Point out each Plasmodium parasite.
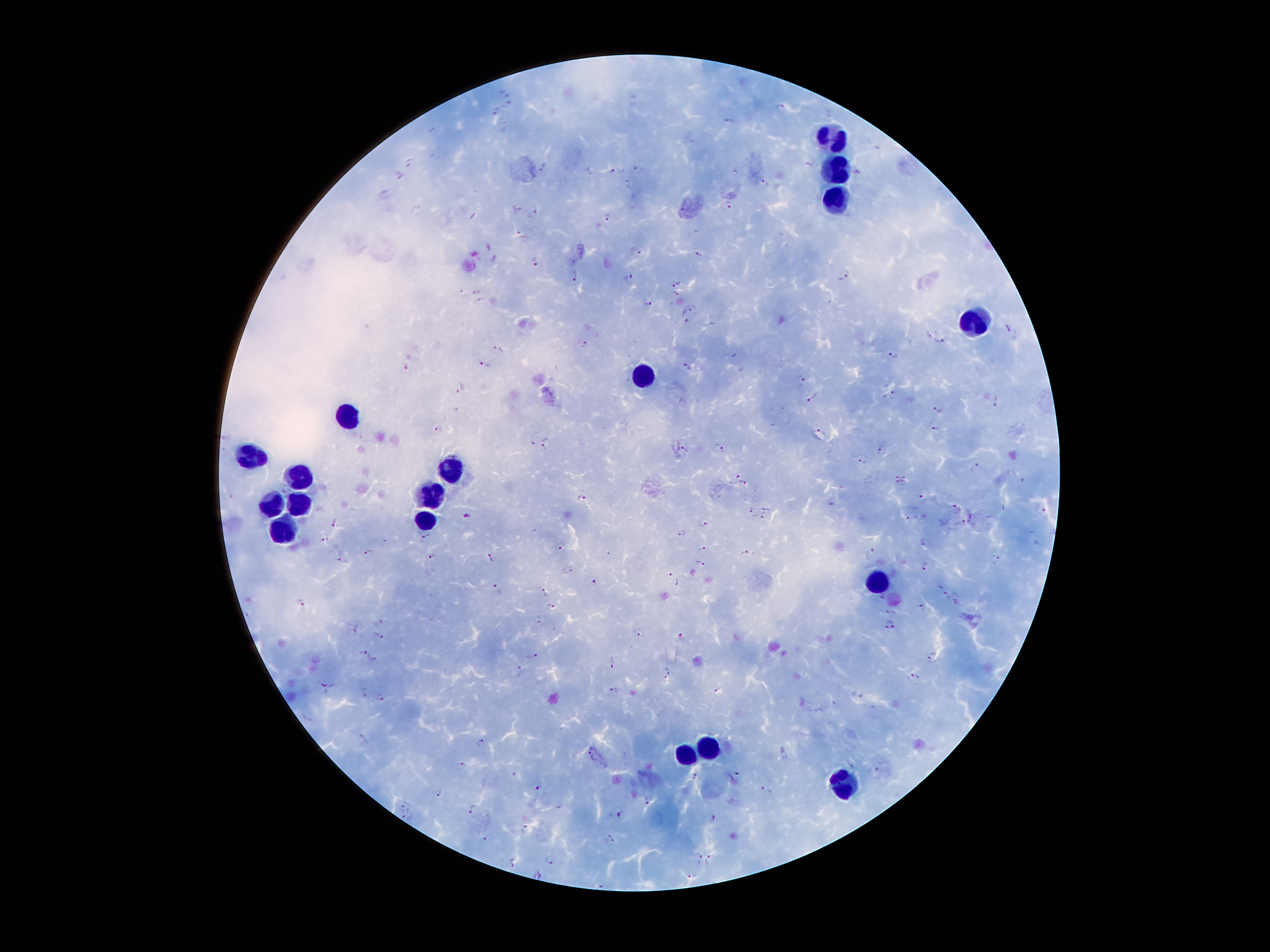
Approximate centers as {x, y} in pixels.
Plasmodium parasites: {506, 92}, {509, 106}, {780, 109}, {495, 111}, {730, 120}, {410, 163}, {810, 164}, {613, 170}, {857, 172}, {764, 182}, {730, 202}, {518, 206}, {535, 210}, {607, 216}, {521, 234}, {638, 252}, {698, 253}, {535, 261}, {844, 272}, {575, 274}, {629, 276}, {676, 283}, {477, 291}, {676, 292}, {649, 303}, {692, 307}, {686, 319}, {943, 341}, {584, 344}, {499, 349}, {894, 355}, {484, 364}, {688, 366}, {405, 367}, {802, 380}, {460, 389}, {894, 394}, {815, 396}, {997, 401}, {939, 407}, {936, 425}, {437, 429}, {818, 432}, {533, 443}, {546, 443}, {719, 446}, {685, 447}, {882, 450}, {863, 457}, {974, 466}, {739, 475}, {900, 478}, {1023, 479}, {744, 483}, {580, 497}, {922, 497}, {832, 502}, {955, 506}, {768, 507}, {1041, 508}, {752, 510}, {468, 515}, {762, 516}, {907, 517}, {333, 521}, {965, 521}, {705, 523}, {681, 533}, {326, 537}, {425, 538}, {924, 542}, {561, 545}, {701, 548}, {874, 548}, {368, 553}, {747, 553}, {432, 555}, {491, 558}, {995, 558}, {343, 560}, {702, 563}, {925, 566}, {569, 569}, {669, 574}, {595, 583}, {498, 589}, {943, 590}, {545, 593}, {883, 596}, {957, 601}, {303, 602}, {551, 604}, {921, 606}, {893, 611}, {539, 618}, {378, 622}, {890, 624}, {355, 628}, {639, 632}, {379, 634}, {680, 636}, {361, 651}, {531, 654}, {933, 656}, {375, 658}, {612, 662}, {521, 671}, {667, 672}, {916, 677}, {328, 685}, {717, 689}, {615, 690}, {363, 692}, {858, 693}, {381, 696}, {364, 738}, {481, 743}, {590, 751}, {461, 763}, {695, 776}, {539, 787}, {767, 789}, {439, 792}, {648, 798}, {403, 804}, {471, 808}, {411, 809}, {619, 814}, {713, 817}, {407, 818}, {526, 828}, {486, 837}, {609, 837}, {696, 855}, {711, 856}, {551, 858}, {513, 862}, {537, 873}, {692, 875}.

Leukocyte locations: {833, 136}, {839, 168}, {838, 193}, {973, 322}, {644, 377}, {348, 418}, {252, 452}, {454, 468}, {295, 477}, {431, 494}, {298, 505}, {268, 506}, {424, 519}, {286, 524}, {876, 578}, {708, 748}, {685, 757}, {849, 784}. Single field of view. 100x magnification. Giemsa-stained preparation. Image is 1270×952 pixels. Patient malaria status: infected with Plasmodium falciparum. Thick blood smear. Smartphone photograph taken through the microscope eyepiece.